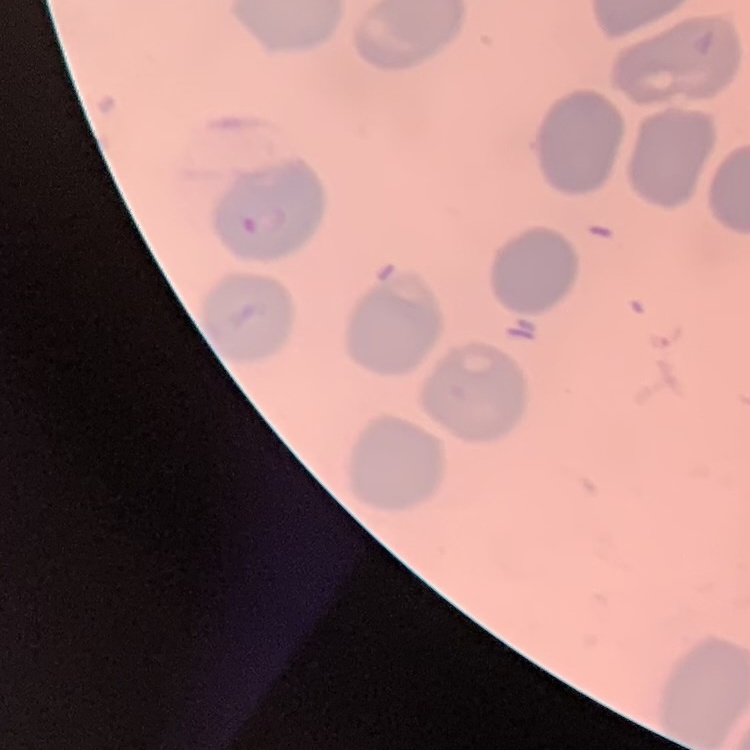
erythrocyte_morphology: no rouleaux formation
preparation: thin peripheral smear
image_type: square crop of a larger photomicrograph
stain: Field's or Giemsa